State the preparation type.
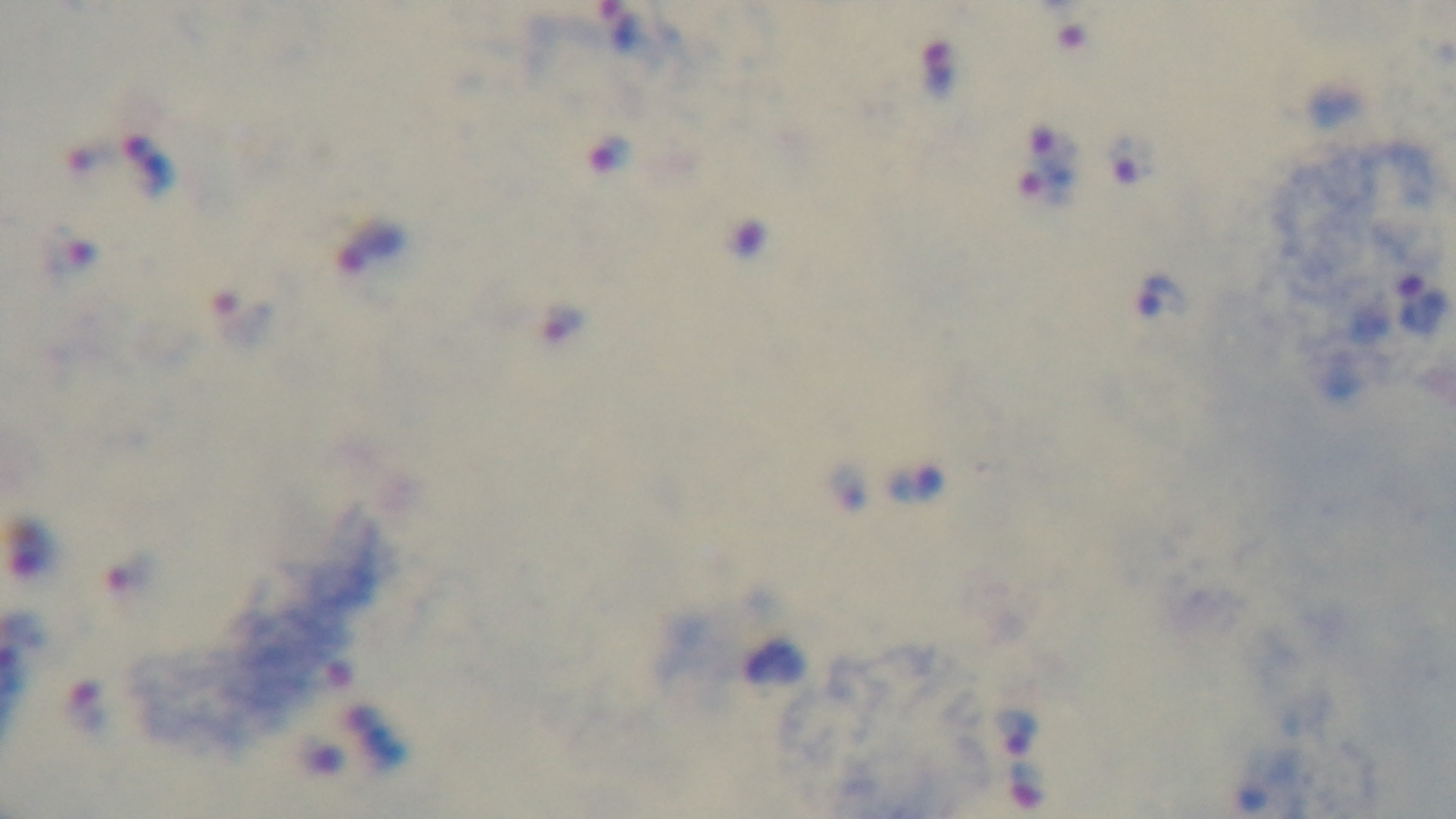
Thick.

field of view = one from the slide
malaria status = infected
modality = light microscopy
capture = mounted 4K digital camera
stain = Giemsa
objective = 100x oil immersion